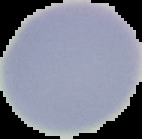

From a thin blood smear. The area outside the segmented cell region is set to black. Result: no Plasmodium parasites detected. Image is 142×139 pixels.